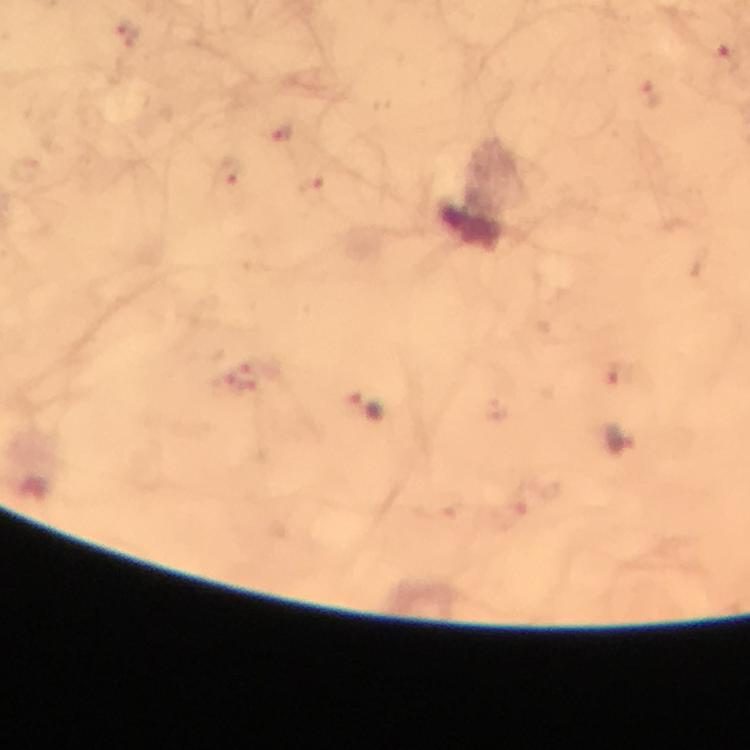
magnification = 100x
image size = 750×750 pixels
stain = Giemsa
capture = smartphone camera through the microscope
immersion oil = used
malaria parasite locations = approximate centers as (x, y) in pixels: (125, 34), (726, 54), (651, 94), (284, 134), (233, 171), (312, 185), (253, 370), (614, 376), (235, 386), (367, 406), (623, 440)
context = from a malaria diagnostic workup
cropped from = one field of view
preparation = thick blood film